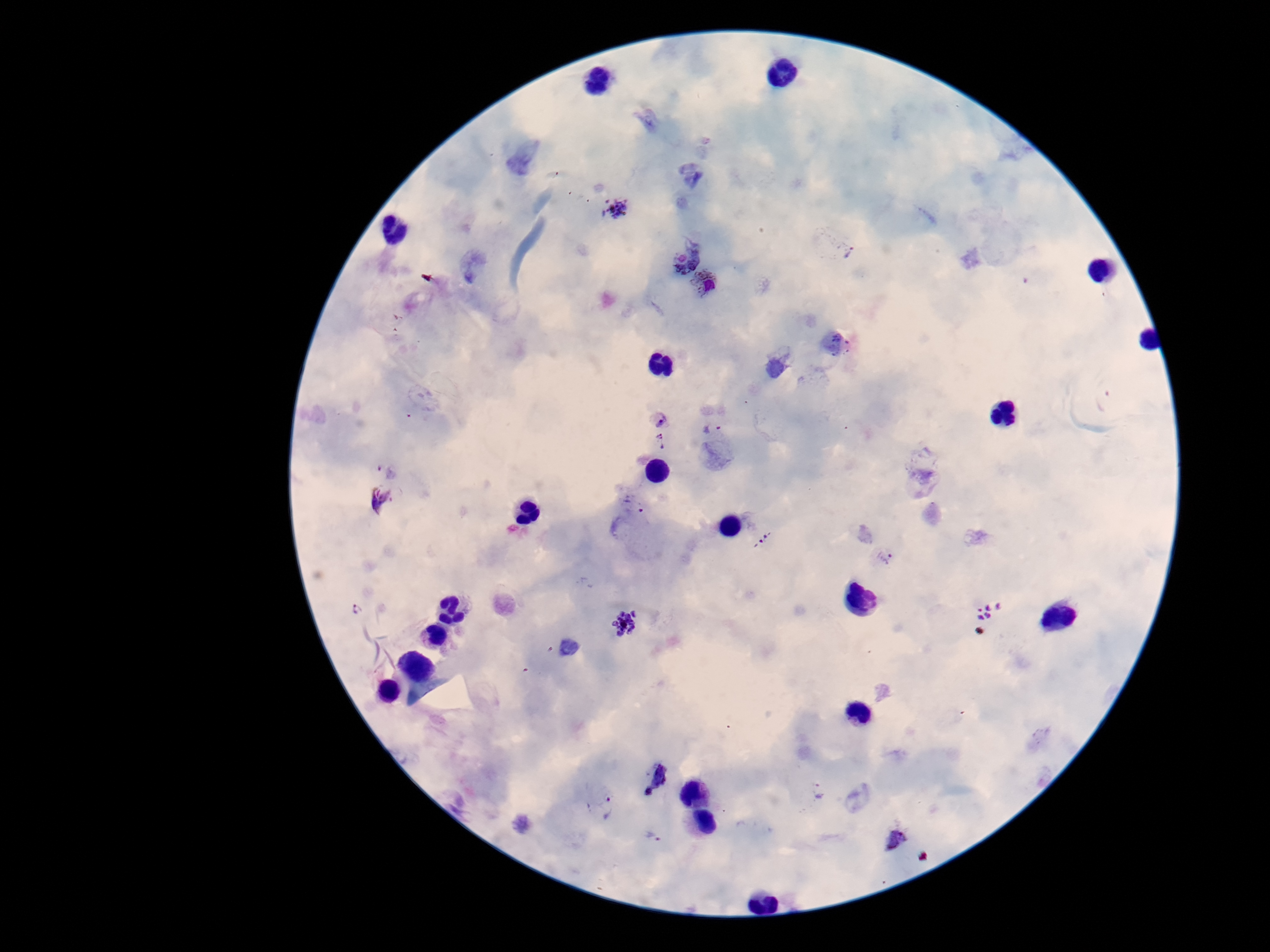
capture: smartphone camera through the microscope eyepiece
stain: Giemsa
field_of_view: one from this slide
plasmodium_parasite_locations: 'approximate centers as {x, y} in pixels: {615, 209}, {839, 246}, {682, 252}, {706, 285}, {661, 418}, {712, 429}, {661, 443}, {387, 465}, {378, 501}, {763, 539}, {885, 557}, {356, 610}, {989, 610}, {626, 624}, {654, 774}, {818, 790}, {602, 807}, {654, 836}, {895, 836}'
patient_malaria_status: infected
magnification: 100x
image_size: 1270×952 pixels
preparation: thick blood smear